Point out leukocytes.
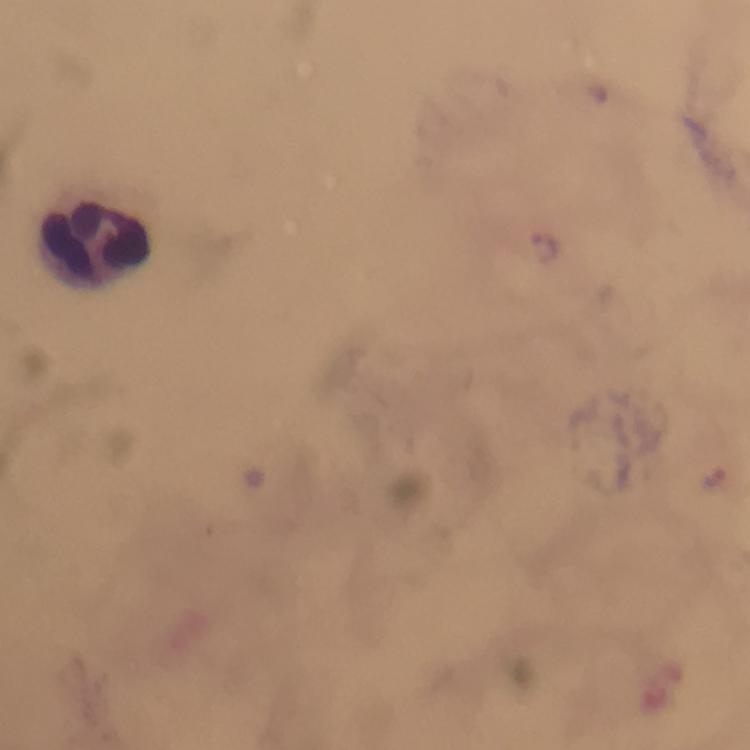

Approximate centers as (x, y) in pixels.
Leukocytes: (99, 244).

stain = Giemsa
image size = 750×750 pixels
Plasmodium parasite locations = approximate centers as (x, y) in pixels: (544, 247), (714, 477)
preparation = thick smear
magnification = 100x
cropped from = one field of view
context = from a diagnostic examination for malaria
capture = smartphone mounted on the microscope
immersion oil = used